Assess the morphology of the erythrocytes.
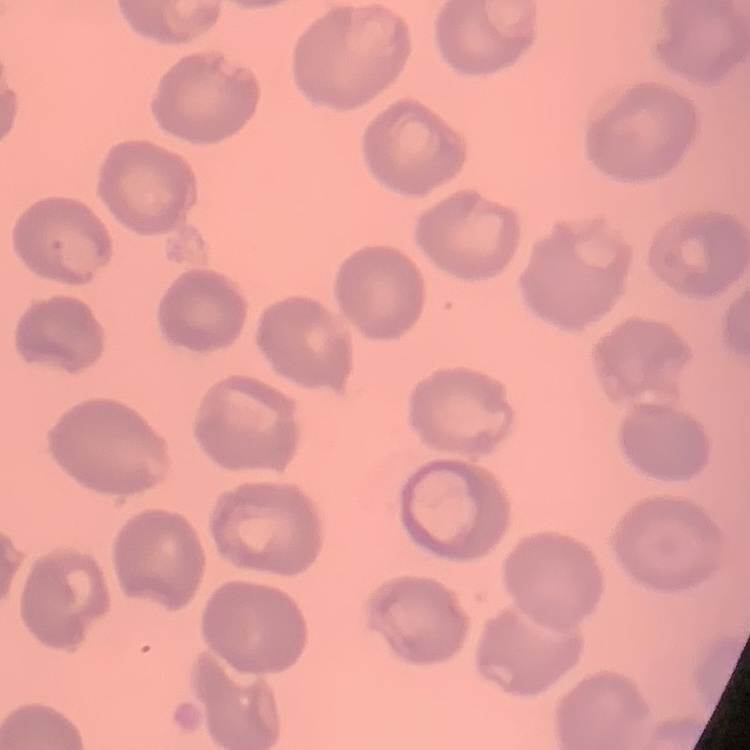
They show no rouleaux formation.

Thin blood smear. Square crop of a larger photomicrograph. Stained with either Field's or Giemsa.